Classify this cell by malaria status.
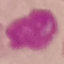
Uninfected.

Summary:
  - Capture: smartphone through the microscope eyepiece
  - Stain: Giemsa
  - Preparation: thin blood smear
  - Image type: automatically extracted cell patch, resized to 64 × 64 pixels